Describe the morphology of the red blood cells.
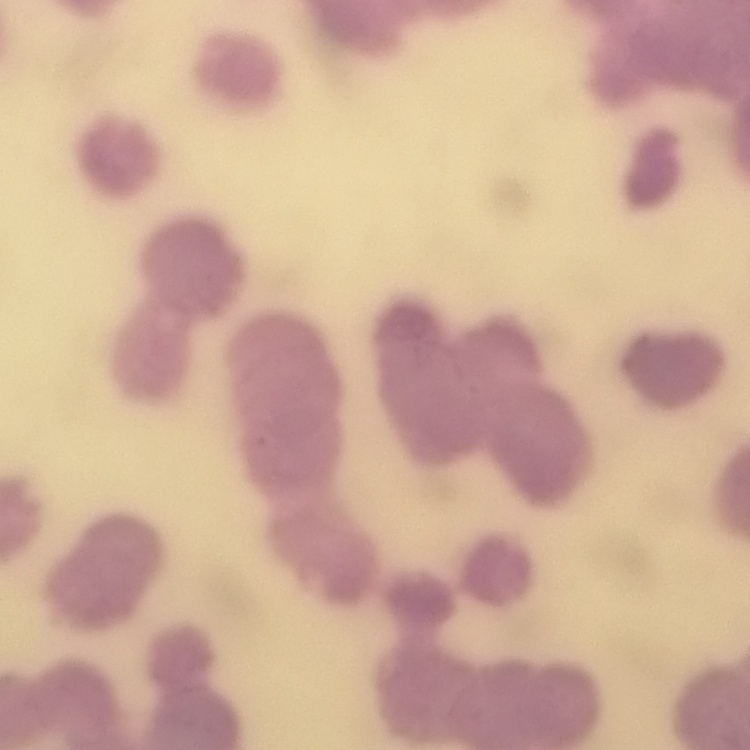

Rouleaux formation.

Summary:
  - Image type: one tile cut from a larger photomicrograph
  - Preparation: thin blood film
  - Stain: Field's or Giemsa